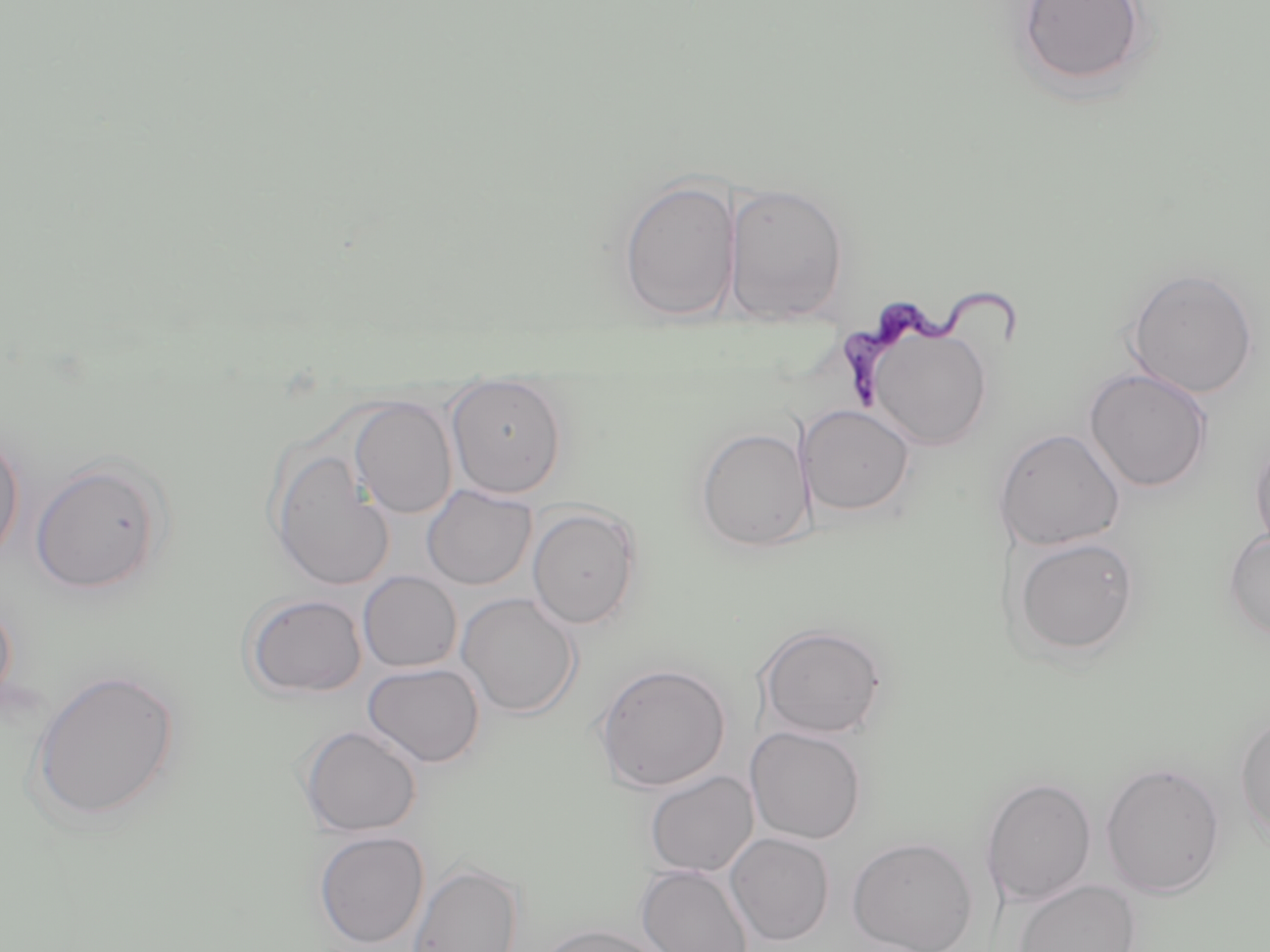
Approximate bounding boxes as (x1, y1, x2, y2) in pixels. Uninfected red blood cell locations: (1014, 0, 1151, 91), (617, 175, 741, 323), (723, 182, 850, 325), (1125, 268, 1259, 398), (867, 326, 993, 450), (1083, 367, 1213, 493), (446, 378, 567, 497), (349, 396, 457, 519), (798, 404, 915, 517), (695, 426, 813, 553), (0, 428, 25, 569), (994, 428, 1125, 551), (1250, 432, 1270, 556), (269, 449, 396, 591), (29, 459, 168, 595), (421, 484, 537, 590), (527, 506, 642, 629), (1223, 529, 1270, 641), (1013, 536, 1140, 658), (357, 571, 462, 673), (242, 592, 367, 699), (456, 593, 581, 718), (0, 596, 17, 711), (757, 623, 888, 740), (363, 662, 485, 768), (594, 662, 731, 792), (28, 668, 182, 826), (1235, 713, 1270, 846), (299, 724, 422, 837), (746, 726, 867, 845), (1100, 761, 1226, 899), (644, 770, 758, 877), (980, 776, 1097, 907), (314, 830, 429, 949), (726, 832, 834, 946), (847, 836, 979, 952), (407, 861, 524, 952), (636, 864, 754, 952), (1013, 879, 1141, 952), (537, 923, 667, 952). Trypanosoma brucei locations: (839, 284, 1024, 410). Slide-level diagnosis: Trypanosoma brucei. One field of a larger specimen. Image is 1270×952 pixels. May-Grünwald-Giemsa-stained preparation. Optical microscopy. Thin blood film. Captured at 1000x magnification.